Comment on the morphology of the erythrocytes.
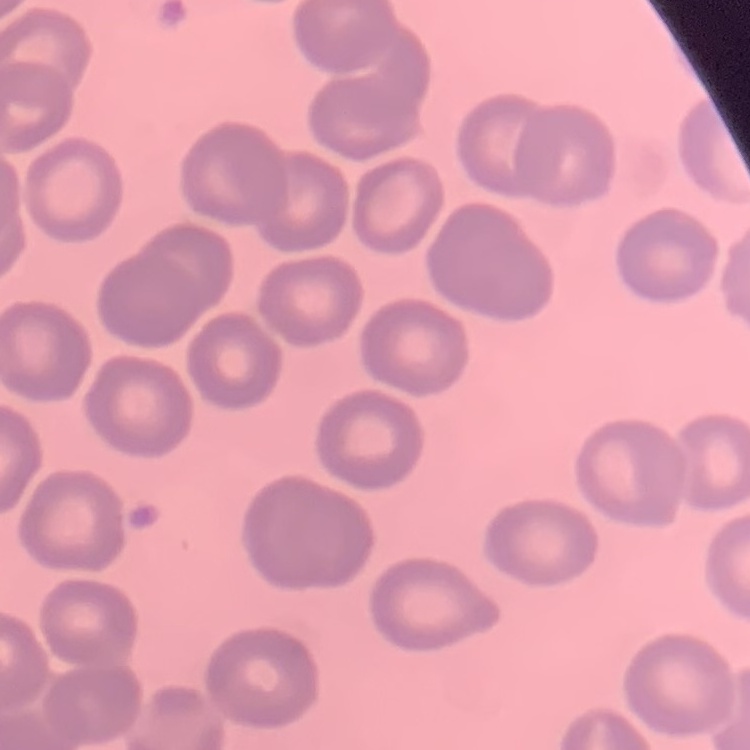

They show no rouleaux formation.

preparation = thin blood film
stain = Field's or Giemsa
image type = one tile cut from a larger photomicrograph